Classify this cell by malaria status.
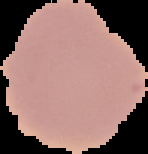
It is uninfected.

image_size: 148×154 pixels
image_type: segmented cell region on a black background
preparation: thin blood film